Classify this cell by malaria status.
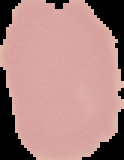

Uninfected.

{
  "preparation": "thin blood film",
  "image_type": "cell region segmented out of the field of view; surrounding area masked to black",
  "image_size": "124×160 pixels"
}